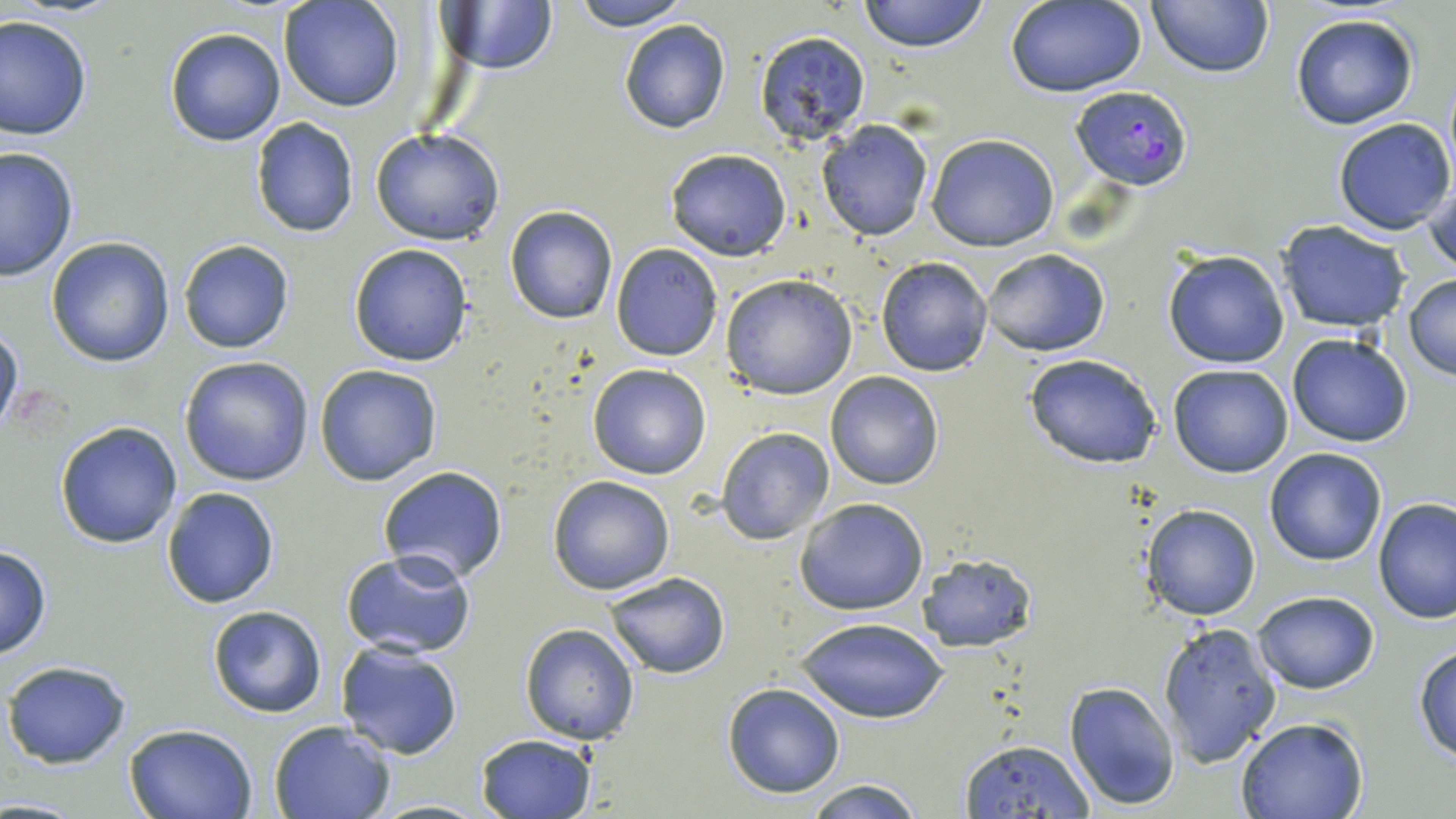
Summary:
  - Coordinate format: approximate bounding boxes as (x1,y1)-(x2,y2) corner pairs in pixels
  - Plasmodium falciparum-infected red blood cell locations: (1070,87)-(1194,191)
  - Uninfected red blood cell locations: (566,0)-(693,30), (856,0)-(989,52), (1146,0)-(1274,79), (279,1)-(404,112), (1005,1)-(1147,96), (437,2)-(559,77), (1291,13)-(1418,130), (0,15)-(91,140), (618,19)-(731,134), (164,27)-(287,147), (754,31)-(872,147), (250,118)-(360,237), (1332,118)-(1454,236), (817,119)-(934,241), (371,128)-(505,246), (925,132)-(1059,251), (0,146)-(78,282), (665,149)-(793,260), (1422,168)-(1455,278), (505,205)-(617,325), (1276,220)-(1412,333), (45,236)-(174,366), (178,240)-(295,354), (348,243)-(474,367), (610,243)-(723,360), (983,249)-(1110,356), (1162,250)-(1290,368), (877,256)-(994,375), (720,274)-(857,399), (1403,274)-(1456,379), (0,322)-(23,438), (1286,332)-(1413,447), (1023,351)-(1163,470), (178,356)-(315,486), (314,363)-(443,485), (588,364)-(712,480), (1168,364)-(1294,478), (825,371)-(943,491), (55,421)-(183,548), (717,427)-(833,544), (1265,447)-(1385,566), (378,466)-(509,586), (548,475)-(675,594), (162,486)-(280,608), (794,497)-(929,615), (1373,497)-(1456,623), (1140,503)-(1261,621), (0,544)-(51,660), (339,549)-(478,658), (916,553)-(1035,652), (603,573)-(730,676), (1252,590)-(1380,693), (206,604)-(327,718), (796,614)-(948,723), (1157,620)-(1285,766), (519,624)-(639,745), (334,640)-(465,758), (1412,645)-(1456,763), (2,659)-(133,768), (1063,681)-(1180,809), (722,683)-(845,797), (1236,716)-(1369,819), (269,720)-(397,819), (124,722)-(260,818), (474,733)-(596,819), (957,738)-(1095,817), (805,779)-(924,818)
  - Slide-level diagnosis: Plasmodium falciparum
  - Magnification: 1000x
  - Image size: 1456×819 pixels
  - Stain: May-Grünwald-Giemsa
  - Modality: optical microscopy
  - Field of view: single
  - Preparation: thin blood smear